State which parasite is depicted.
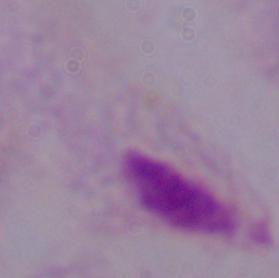
This is a trichomonad.

magnification = 1000x
modality = micrograph